Name the blood parasite species.
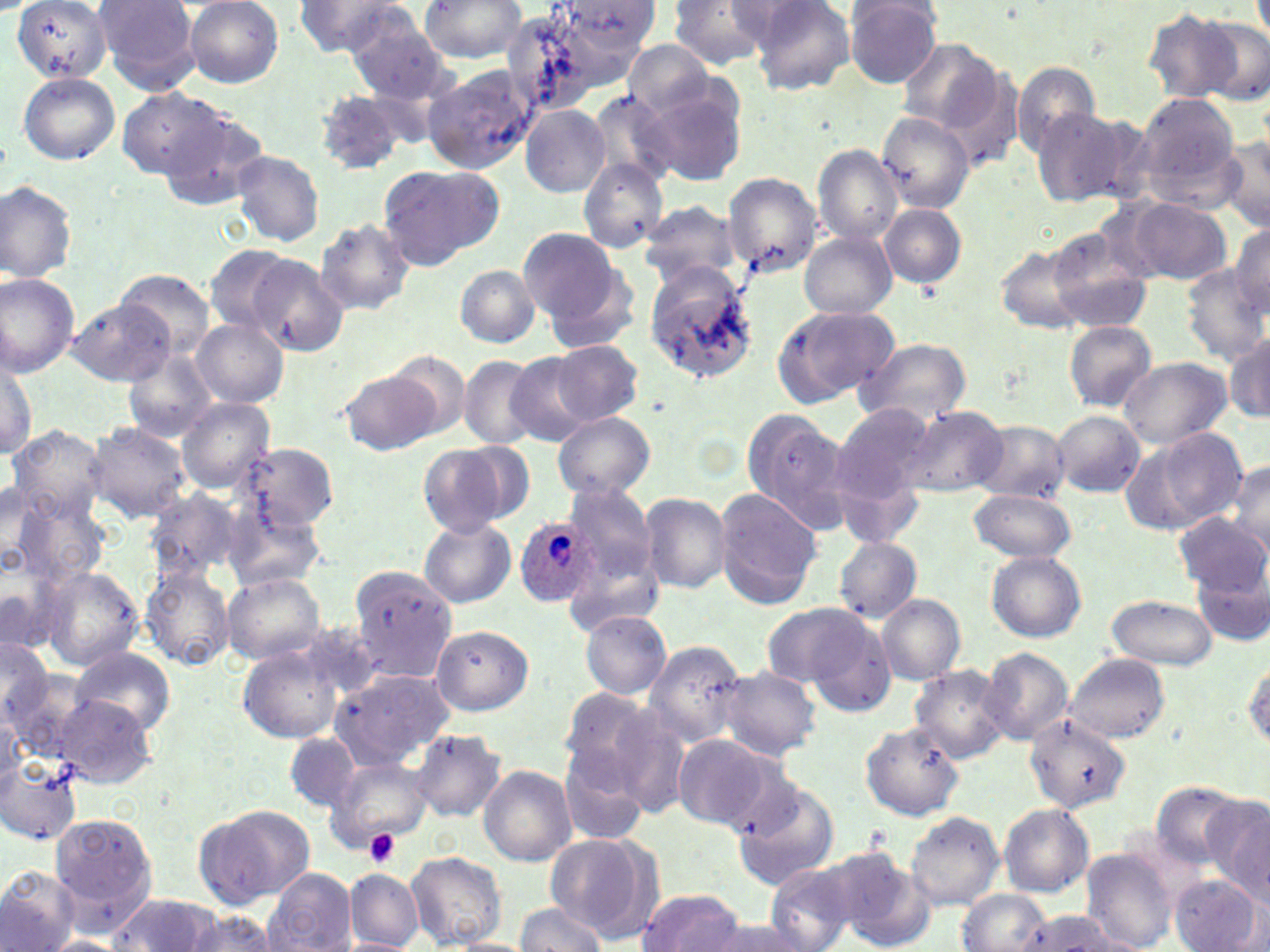

Plasmodium ovale.

Approximate bounding boxes as [x1, y1, x2, y2] in pixels. Plasmodium ovale-infected red blood cell locations: [513, 514, 600, 606]. Uninfected red blood cell locations: [93, 0, 200, 93], [296, 0, 415, 57], [418, 0, 528, 64], [747, 0, 856, 94], [10, 1, 114, 84], [182, 1, 284, 87], [559, 1, 662, 56], [667, 1, 771, 71], [842, 1, 944, 87], [498, 7, 614, 116], [1143, 7, 1242, 104], [1195, 9, 1270, 104], [347, 16, 457, 110], [895, 38, 1002, 137], [625, 41, 717, 117], [1011, 59, 1104, 158], [424, 67, 540, 173], [18, 73, 120, 165], [639, 85, 748, 185], [119, 87, 228, 179], [590, 90, 677, 188], [315, 92, 411, 179], [1134, 92, 1243, 200], [520, 105, 610, 197], [1030, 106, 1145, 209], [158, 109, 271, 213], [878, 113, 974, 213], [1217, 137, 1270, 233], [813, 144, 904, 246], [231, 150, 324, 246], [579, 158, 669, 253], [378, 165, 497, 269], [722, 171, 822, 276], [0, 181, 77, 283], [1129, 198, 1232, 284], [635, 200, 743, 290], [880, 203, 966, 290], [315, 219, 415, 314], [1228, 222, 1270, 321], [518, 227, 621, 325], [1045, 228, 1154, 332], [799, 231, 896, 319], [996, 244, 1089, 332], [203, 245, 296, 333], [245, 254, 351, 357], [643, 261, 760, 386], [456, 265, 540, 347], [1182, 267, 1267, 364], [115, 269, 215, 359], [0, 273, 80, 377], [69, 297, 173, 385], [771, 304, 898, 407], [193, 319, 288, 407], [1064, 321, 1156, 411], [1227, 330, 1270, 422], [857, 338, 972, 428], [549, 342, 642, 426], [124, 349, 215, 442], [389, 350, 472, 437], [504, 351, 601, 446], [1, 353, 37, 459], [1118, 356, 1232, 449], [457, 357, 541, 449], [339, 370, 440, 455], [177, 397, 276, 492], [832, 404, 936, 505], [899, 404, 1008, 497], [739, 410, 852, 535], [1051, 411, 1146, 497], [554, 412, 655, 500], [971, 420, 1070, 501], [86, 422, 193, 522], [7, 425, 109, 528], [1120, 428, 1248, 536], [237, 442, 338, 531], [418, 442, 520, 538], [1226, 460, 1269, 555], [838, 474, 920, 554], [562, 481, 657, 586], [3, 484, 51, 578], [712, 488, 822, 610], [143, 489, 245, 586], [968, 489, 1080, 563], [7, 490, 106, 586], [642, 492, 731, 592], [225, 502, 324, 594], [1176, 512, 1267, 596], [418, 518, 514, 608], [833, 536, 923, 622], [565, 547, 663, 637], [987, 551, 1086, 641], [1195, 562, 1270, 646], [35, 564, 144, 672], [139, 564, 234, 670], [348, 565, 455, 682], [222, 572, 326, 666], [878, 593, 965, 683], [1105, 595, 1219, 670], [759, 601, 876, 690], [580, 610, 671, 700], [803, 615, 898, 716], [430, 625, 533, 716], [0, 637, 54, 727], [645, 637, 750, 747], [239, 644, 348, 743], [68, 647, 177, 738], [979, 648, 1074, 746], [1066, 653, 1171, 744], [1243, 657, 1270, 752], [2, 666, 88, 761], [911, 666, 1010, 761], [719, 667, 820, 759], [329, 670, 453, 770], [557, 688, 660, 784], [51, 693, 159, 786], [0, 709, 27, 792], [1025, 718, 1132, 813], [860, 723, 964, 821], [412, 729, 508, 822], [284, 731, 360, 812], [671, 733, 777, 832], [557, 748, 650, 847], [0, 754, 84, 846], [325, 755, 430, 852], [479, 764, 576, 865], [732, 777, 840, 889], [1152, 782, 1247, 867], [1200, 796, 1270, 894], [999, 803, 1093, 896], [193, 805, 312, 908], [905, 810, 1005, 910], [52, 811, 161, 928], [545, 833, 657, 938], [1084, 848, 1181, 951], [828, 849, 933, 951], [404, 851, 507, 948], [762, 861, 862, 952], [0, 865, 77, 952], [264, 868, 356, 952], [345, 869, 423, 951], [1169, 874, 1264, 952], [638, 888, 746, 951], [958, 890, 1048, 952], [107, 893, 218, 951], [513, 902, 607, 952], [1018, 910, 1116, 952], [180, 911, 282, 952], [703, 919, 817, 952], [42, 936, 127, 951], [441, 937, 538, 952]. Platelet locations: [365, 829, 400, 867]. May-Grünwald-Giemsa stain. Single field of view. Image is 1270×952 pixels. Optical microscopy. 1000x magnification. Thin blood film.